Name the cell type shown.
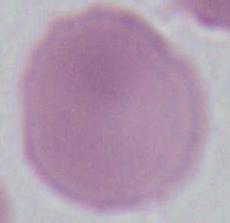

An erythrocyte.

Micrograph. Captured at 1000x magnification.